Assess the morphology of the erythrocytes.
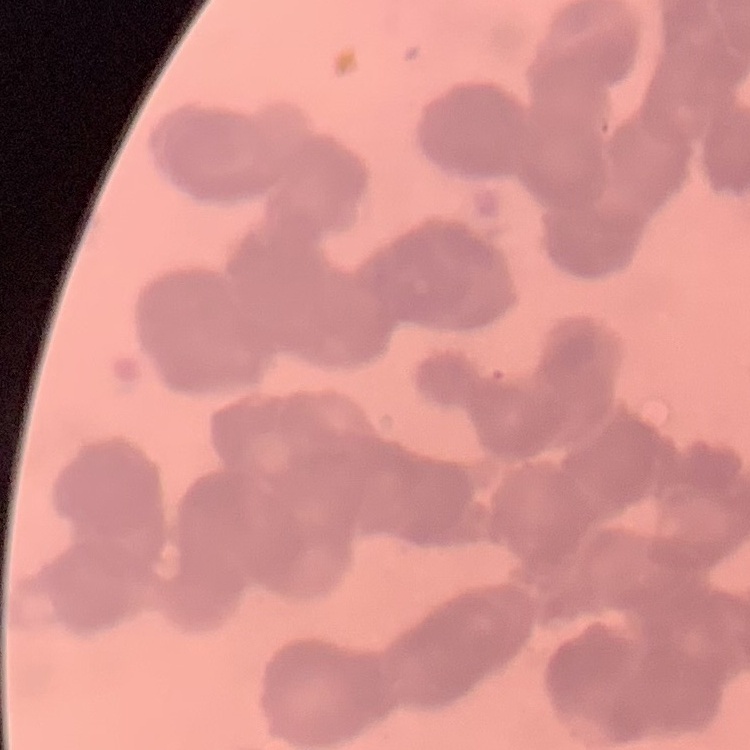
Rouleaux formation.

image_type: one tile cut from a larger photomicrograph
preparation: thin peripheral smear
stain: Field's or Giemsa